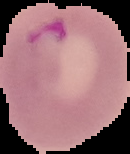

Segmented cell region on a black background. From a thin blood film. Image is 130×154 pixels. Malaria status: parasitized.